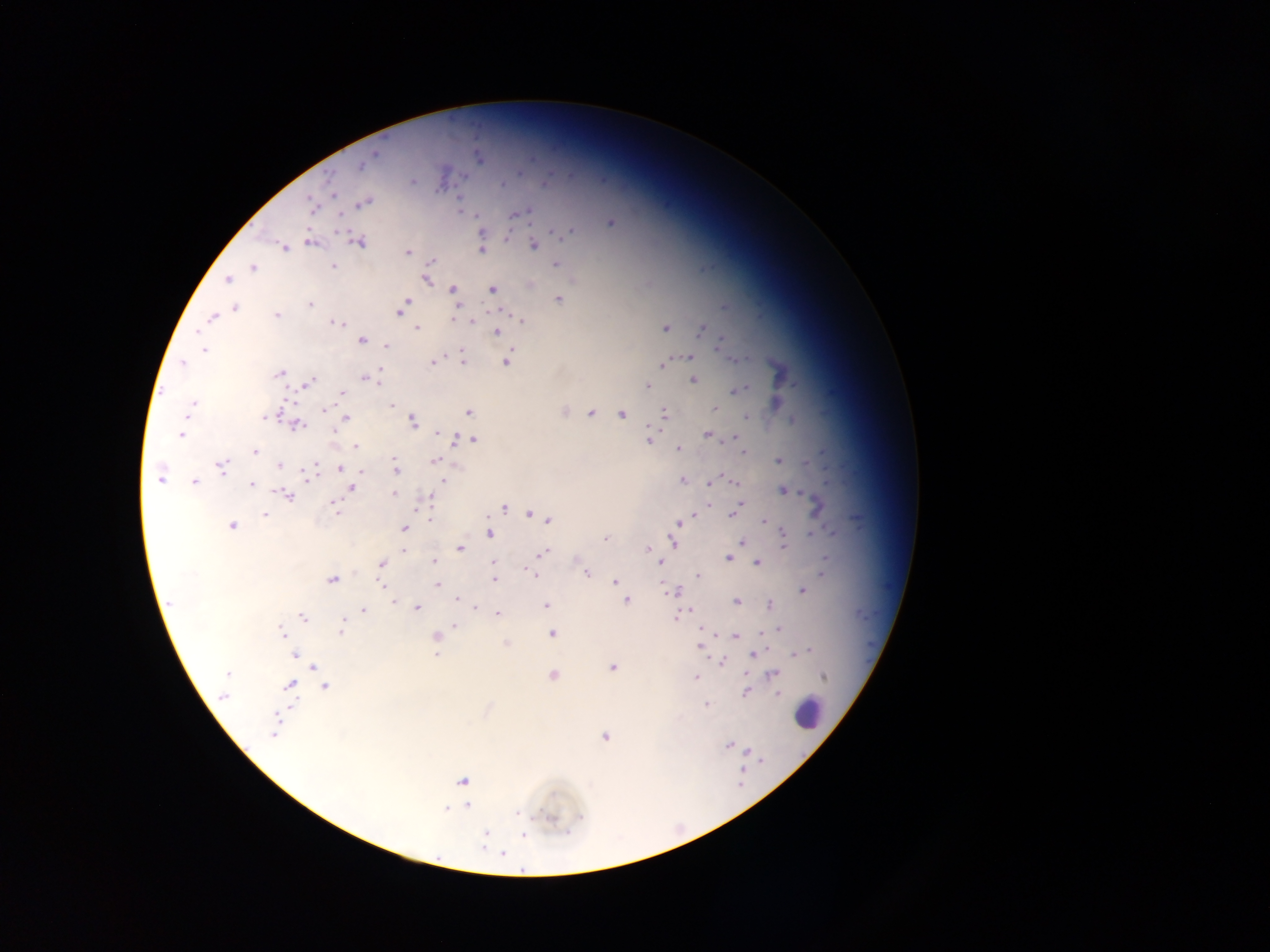
Approximate centers as (x, y) in pixels. Leukocyte locations: (807, 712). Malaria parasite locations: (373, 154), (479, 158), (361, 165), (413, 181), (502, 184), (329, 193), (363, 203), (311, 205), (519, 213), (610, 222), (480, 231), (569, 231), (556, 233), (506, 239), (310, 241), (359, 241), (534, 245), (284, 247), (480, 249), (407, 252), (431, 260), (556, 263), (332, 265), (253, 267), (426, 278), (227, 280), (529, 285), (452, 288), (492, 288), (559, 299), (405, 303), (310, 304), (236, 307), (458, 308), (400, 310), (276, 314), (212, 317), (454, 319), (522, 321), (339, 323), (665, 327), (415, 328), (701, 329), (496, 332), (362, 340), (721, 343), (385, 346), (203, 350), (689, 356), (733, 359), (433, 360), (463, 360), (505, 360), (183, 363), (663, 364), (279, 373), (377, 373), (364, 377), (693, 379), (376, 382), (306, 383), (647, 386), (743, 387), (737, 390), (342, 394), (191, 404), (392, 406), (324, 408), (715, 408), (188, 410), (564, 411), (468, 412), (591, 413), (664, 413), (622, 414), (268, 415), (745, 416), (345, 418), (793, 419), (412, 421), (296, 425), (649, 427), (439, 432), (182, 434), (708, 435), (468, 438), (472, 438), (733, 438), (457, 439), (648, 439), (354, 445), (678, 449), (254, 452), (743, 453), (435, 460), (779, 460), (394, 461), (806, 463), (280, 465), (221, 466), (340, 469), (396, 469), (360, 470), (309, 473), (159, 478), (442, 479), (682, 480), (194, 482), (733, 482), (710, 483), (251, 484), (351, 488), (782, 489), (393, 494), (288, 495), (428, 496), (710, 503), (741, 503), (816, 505), (334, 506), (738, 506), (503, 507), (529, 513), (265, 514), (695, 514), (733, 514), (430, 519), (548, 520), (764, 521), (678, 523), (232, 525), (404, 528), (490, 533), (812, 535), (605, 539), (674, 541), (743, 542), (783, 546), (460, 548), (647, 549), (403, 550), (543, 553), (728, 558), (824, 559), (433, 561), (493, 562), (662, 562), (758, 562), (381, 564), (586, 572), (535, 574), (698, 574), (822, 574), (493, 579), (332, 580), (614, 581), (437, 584), (618, 585), (663, 586), (802, 590), (678, 591), (457, 598), (393, 600), (626, 601), (736, 601), (169, 603), (768, 604), (546, 606), (417, 607), (363, 610), (682, 612), (497, 614), (676, 616), (303, 619), (343, 622), (455, 625), (778, 628), (701, 629), (341, 630), (762, 632), (282, 633), (551, 633), (436, 637), (735, 637), (506, 643), (700, 646), (808, 649), (796, 652), (438, 653), (753, 653), (296, 655), (720, 662), (315, 667), (612, 667), (228, 673), (772, 674), (552, 675), (747, 676), (822, 676), (695, 678), (291, 684), (325, 687), (746, 691), (778, 694), (223, 695), (706, 704), (275, 730), (605, 736), (727, 744), (462, 780), (467, 805), (517, 812), (485, 833), (522, 836), (503, 854). Sample from Ghana. Image is 1270×952 pixels. Single field of view. Mobile-phone photograph taken through the microscope. Thick blood film.